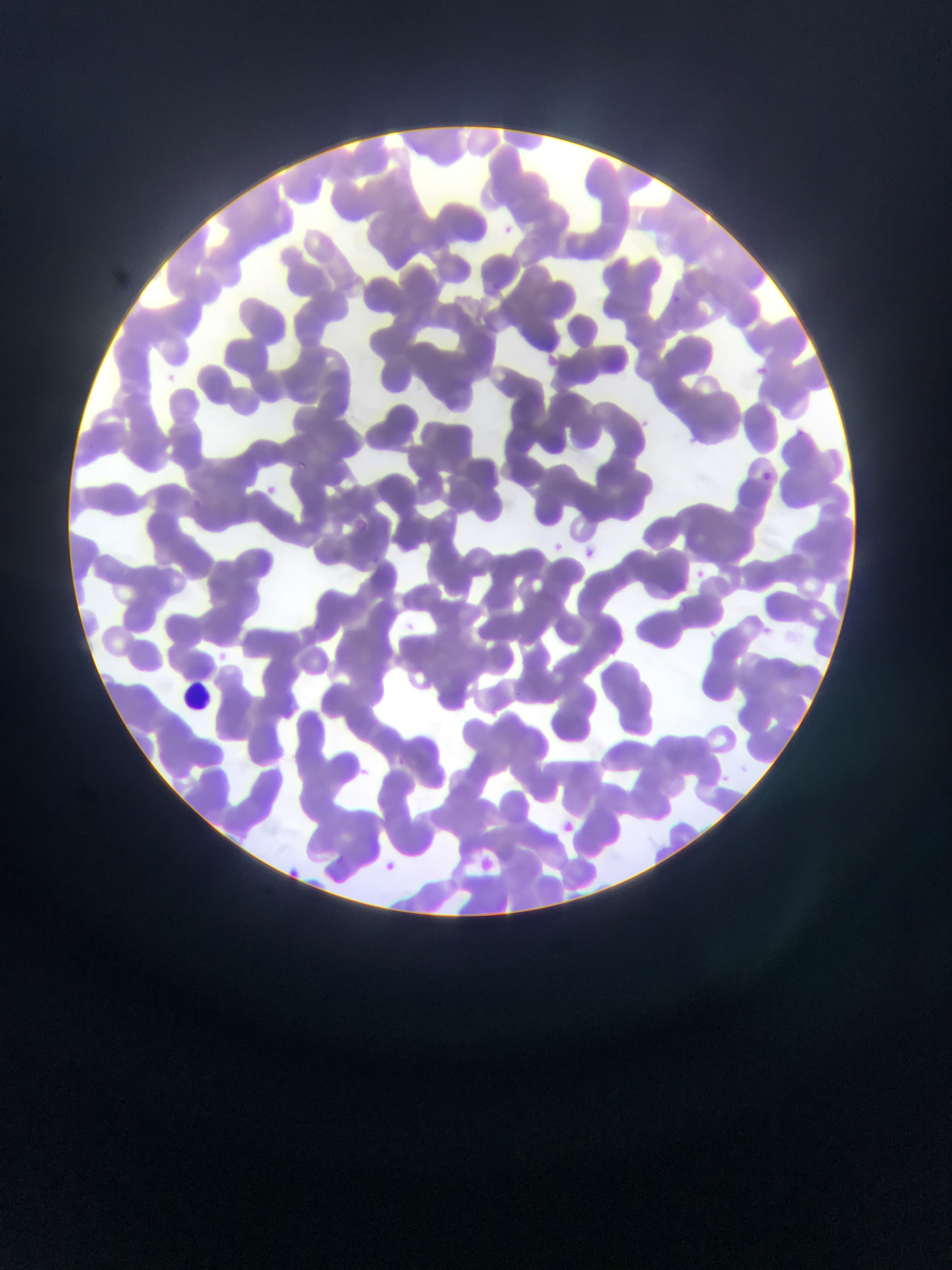
Approximate bounding boxes as (left, top, right, bottom) in pixels.
Summary:
  - Leukocyte locations: (179, 680, 214, 715)
  - Plasmodium parasite locations: (502, 220, 517, 233), (488, 280, 501, 292), (673, 295, 681, 303), (544, 352, 559, 365), (746, 363, 773, 377), (169, 373, 174, 381), (642, 415, 652, 427), (299, 457, 310, 470), (762, 472, 771, 481), (264, 483, 284, 496), (354, 518, 370, 534), (552, 538, 566, 550), (580, 542, 599, 557), (693, 564, 708, 581), (676, 601, 686, 611), (313, 622, 321, 632), (762, 623, 776, 637), (359, 762, 376, 785), (559, 810, 577, 838), (471, 853, 497, 874), (385, 858, 401, 865), (285, 863, 307, 877)
  - Capture: mobile-phone photograph through a microscope
  - Country: Ghana
  - Preparation: thin blood smear
  - Image size: 952×1270 pixels
  - Field of view: single